Identify the preparation type.
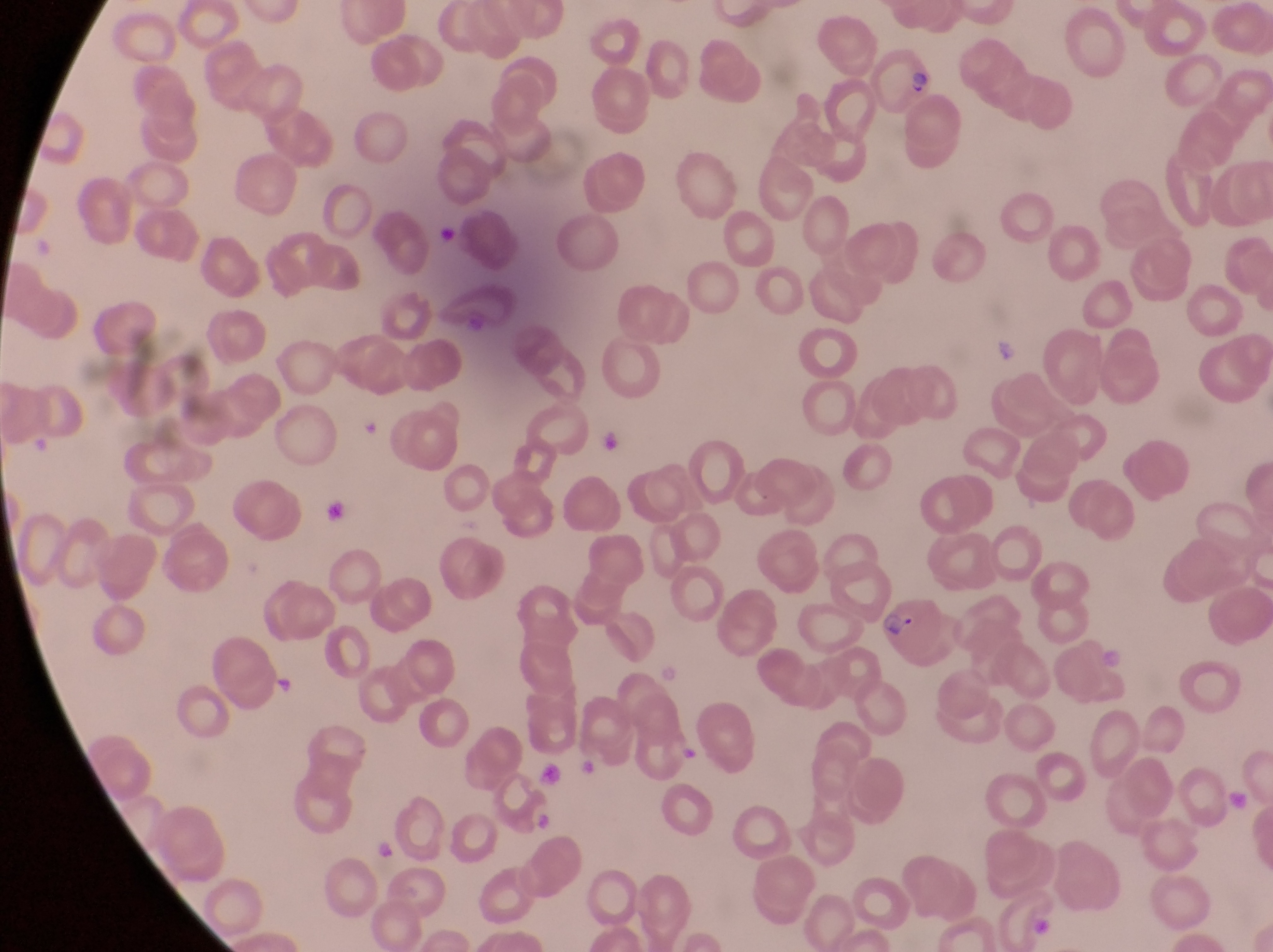

Thin blood smear.

Approximate bounding boxes as (left, top, right, bottom) in pixels.
Summary:
  - Parasitised red blood cell locations: (869, 43, 936, 115), (876, 599, 963, 669)
  - Artifact (platelet-like body, stain precipitate, or debris) locations: (436, 225, 463, 251), (596, 427, 629, 470), (320, 492, 359, 535), (532, 759, 565, 787), (532, 814, 556, 834), (374, 839, 398, 862)
  - Trophozoite locations: (989, 335, 1022, 370)
  - Image size: 1273×952 pixels
  - Magnification: 1000x
  - Field of view: single
  - Capture: smartphone photograph through the eyepiece of an Olympus CX-23 microscope
  - Country: Uganda